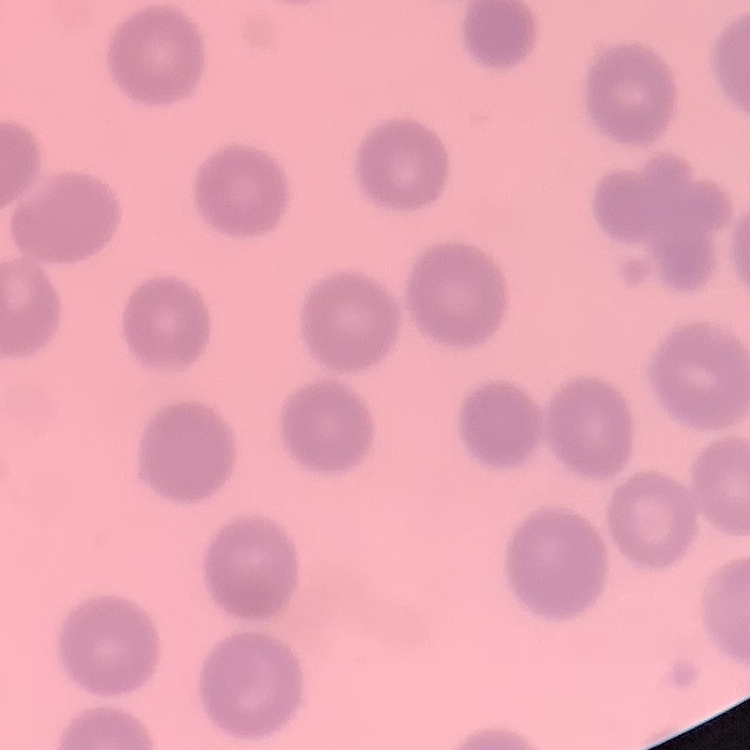 The erythrocytes exhibit no rouleaux formation. Stained with either Field's or Giemsa. One tile cut from a larger photomicrograph. Thin blood film.